Assess the morphology of the red blood cells.
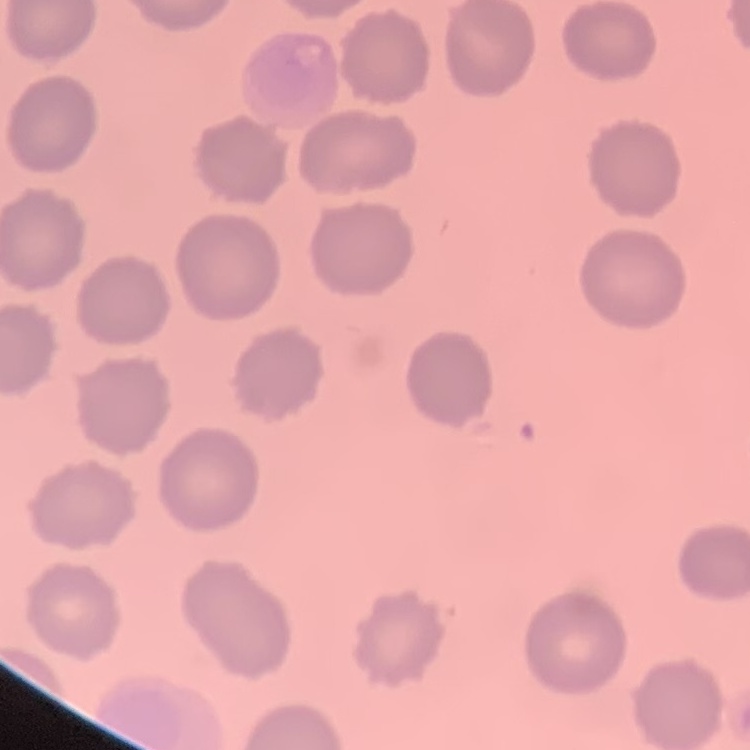

They show no rouleaux formation.

preparation = thin blood film
image type = square crop of a larger photomicrograph
stain = Field's or Giemsa